State which cell type is depicted.
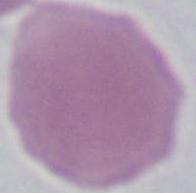
An erythrocyte.

Captured at 1000x magnification. Micrograph.